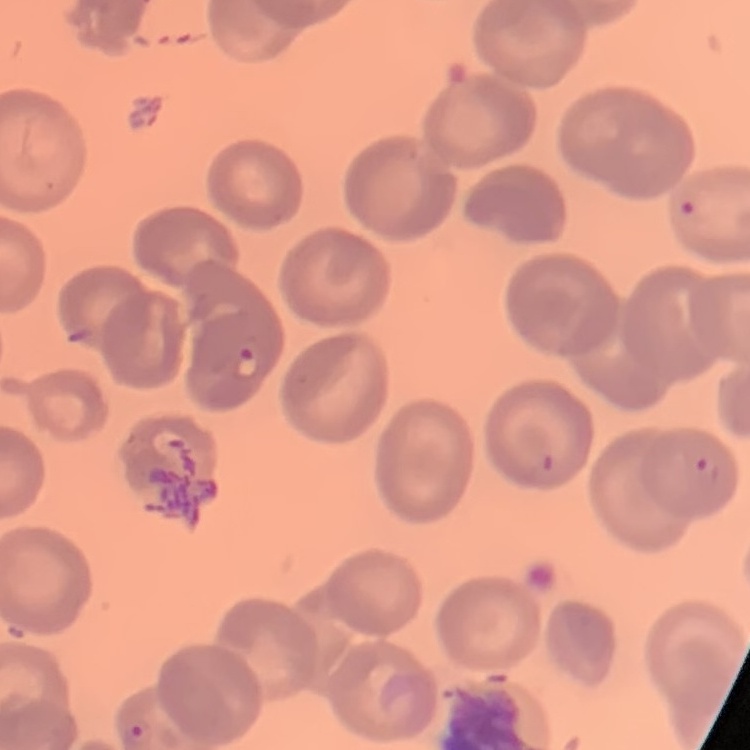

Summary:
  - Erythrocyte morphology: no rouleaux formation
  - Stain: Field's or Giemsa
  - Preparation: thin peripheral smear
  - Image type: one tile cut from a larger photomicrograph